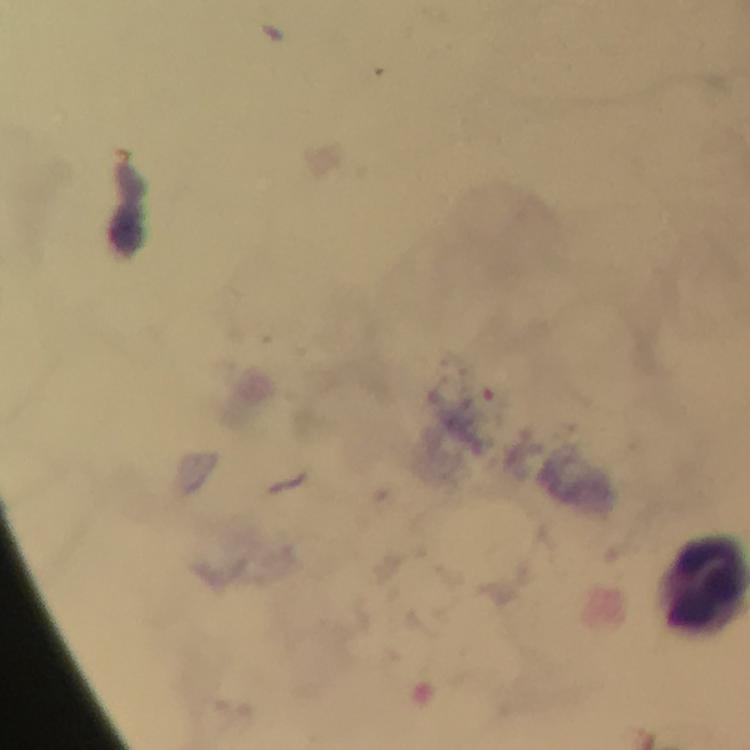

context = from a malaria diagnostic workup
capture = smartphone mounted on the microscope
magnification = 100x
immersion oil = used
image size = 750×750 pixels
cropped from = one field of view
preparation = thick smear
stain = Giemsa
malaria parasite locations = approximate centers as {x, y} in pixels: {490, 404}